Name the parasite shown.
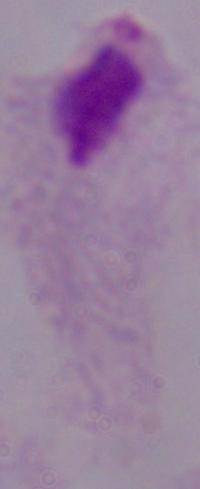
A trichomonad.

Summary:
  - Modality: micrograph
  - Magnification: 1000x